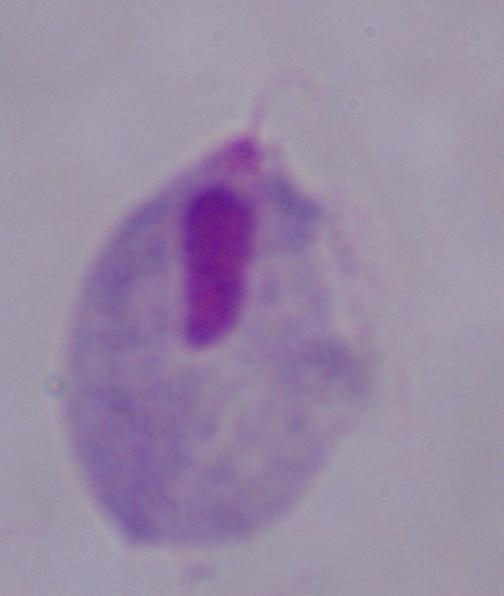
Captured at 1000x magnification. A trichomonad is seen. Micrograph.